Identify the parasite.
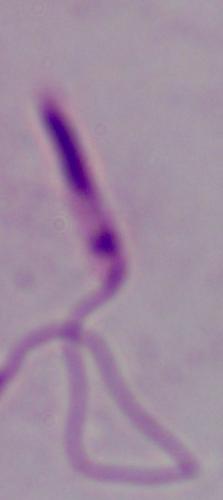
Leishmania.

Photomicrograph. Captured at 1000x magnification.